State which cell type is depicted.
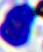

This is a leukocyte.

Summary:
  - Magnification: 400x
  - Modality: micrograph